Assess this cell for malaria.
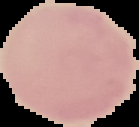
Uninfected.

From a thin blood film. Image is 139×127 pixels. Cell region segmented out of the field of view; the surrounding area is masked to black.